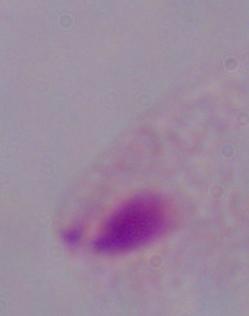 Photomicrograph. 1000x magnification. A trichomonad is seen.